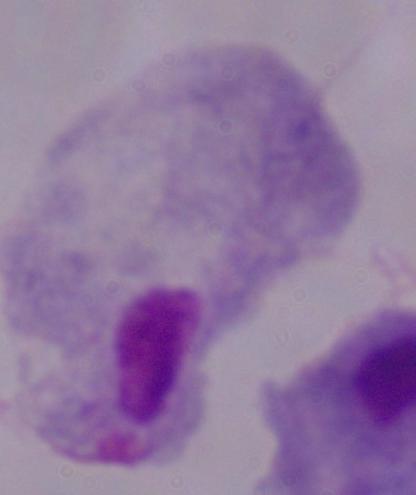

modality = photomicrograph
identification = trichomonad
magnification = 1000x